Comment on the morphology of the red blood cells.
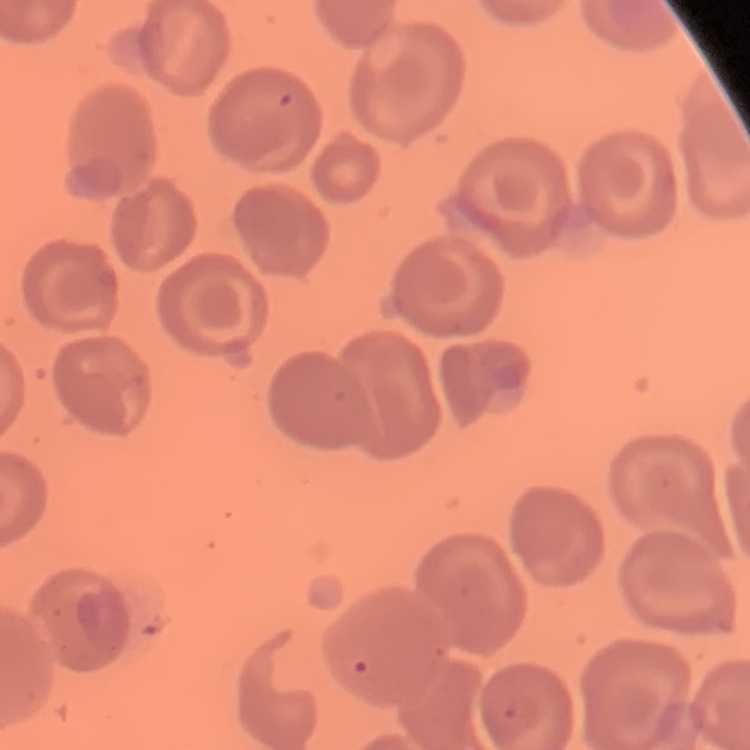

No rouleaux formation.

Summary:
  - Preparation: thin blood film
  - Image type: square crop of a larger photomicrograph
  - Stain: Field's or Giemsa